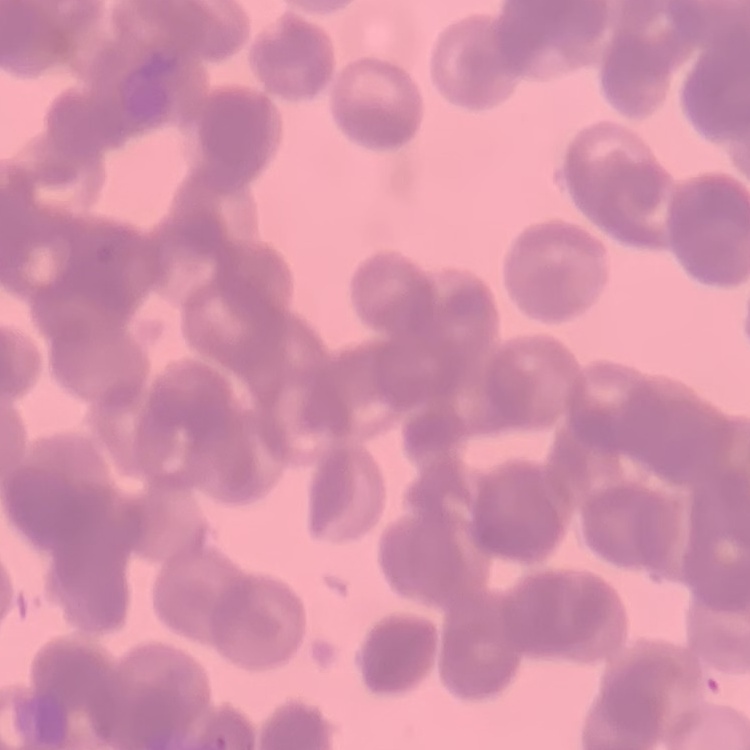 The red blood cells show rouleaux formation. Stained with either Field's or Giemsa. One tile cut from a larger photomicrograph. Thin peripheral smear.